Comment on the morphology of the erythrocytes.
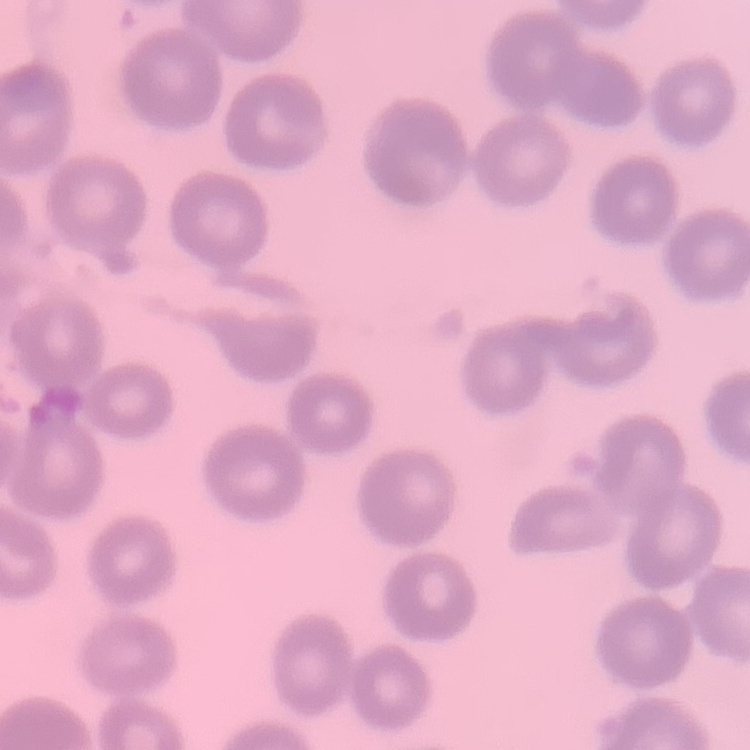

No rouleaux formation.

Stained with either Field's or Giemsa. Square crop of a larger photomicrograph. Thin blood smear.